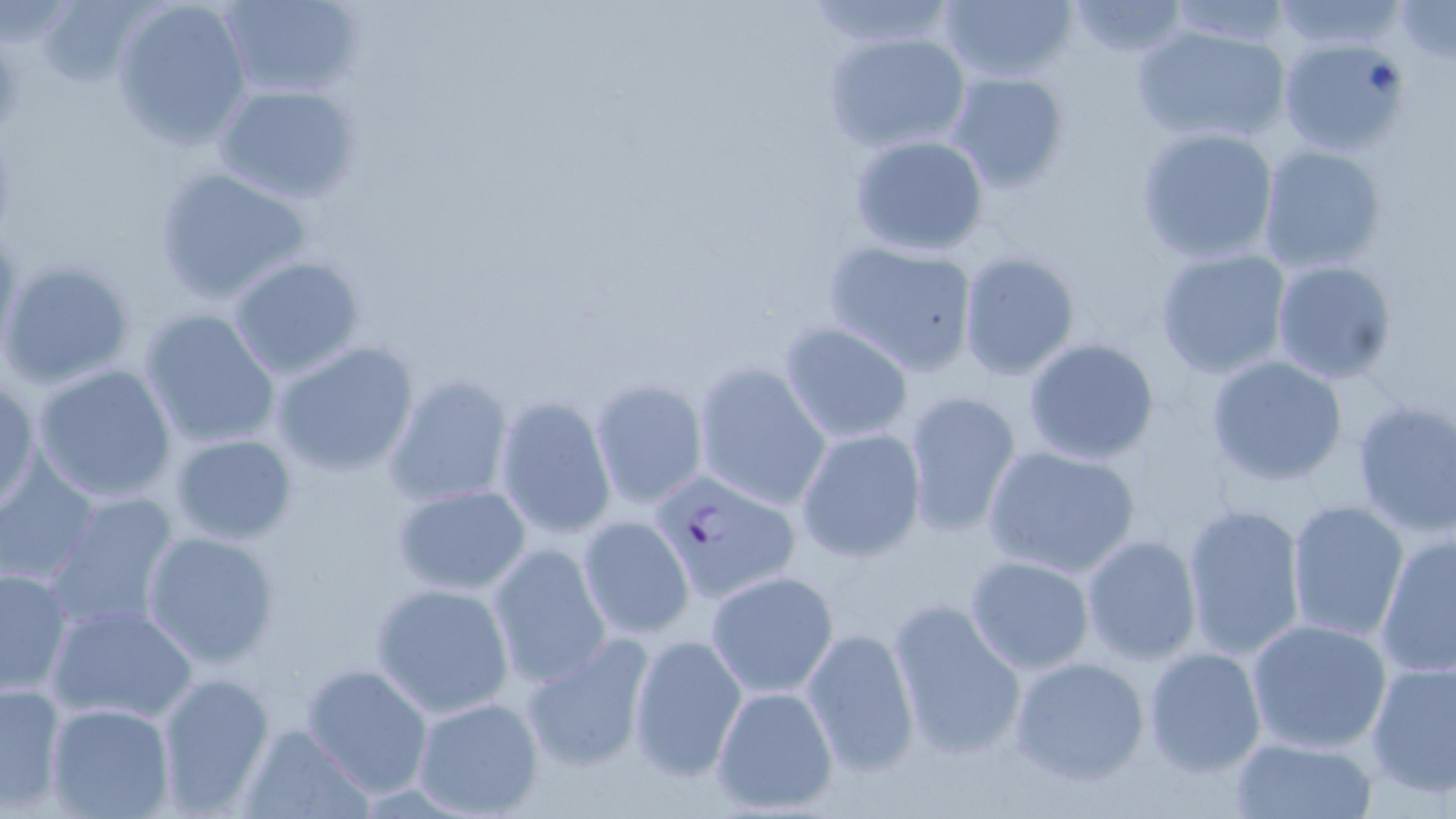

Summary:
  - Coordinate format: approximate bounding boxes as (x1,y1)-(x2,y2) corner pairs in pixels
  - Uninfected red blood cell locations: (110,0)-(254,150), (215,0)-(365,103), (935,0)-(1079,85), (802,1)-(961,51), (1061,1)-(1192,57), (1161,1)-(1297,49), (1267,1)-(1406,51), (1393,2)-(1456,66), (32,3)-(152,91), (1130,23)-(1291,149), (822,30)-(973,155), (1277,38)-(1410,157), (1,43)-(29,134), (945,70)-(1072,195), (212,82)-(361,204), (1134,125)-(1280,266), (847,132)-(991,259), (1256,144)-(1389,274), (153,164)-(317,304), (821,238)-(982,375), (1153,247)-(1294,379), (957,250)-(1082,381), (227,254)-(366,380), (1269,261)-(1398,384), (139,308)-(282,450), (778,321)-(916,445), (1022,337)-(1163,467), (270,340)-(420,479), (1205,354)-(1349,488), (693,364)-(831,509), (32,365)-(178,504), (383,374)-(516,509), (0,378)-(38,512), (590,379)-(707,508), (901,389)-(1023,538), (492,395)-(617,539), (1349,397)-(1456,538), (794,427)-(926,563), (168,432)-(299,543), (981,443)-(1142,577), (0,459)-(101,587), (392,483)-(533,595), (43,490)-(182,637), (1286,499)-(1410,645), (1182,503)-(1307,662), (578,516)-(694,640), (140,529)-(282,669), (1375,532)-(1456,679), (1080,535)-(1202,665), (488,542)-(613,688), (965,554)-(1095,674), (0,566)-(73,699), (705,569)-(839,698), (370,582)-(516,717), (886,597)-(1028,761), (46,602)-(199,726), (1246,619)-(1393,755), (801,626)-(920,776), (519,633)-(657,774), (625,633)-(748,781), (1141,646)-(1268,777), (1008,654)-(1150,788), (1365,659)-(1456,797), (299,662)-(435,799), (152,670)-(276,815), (0,681)-(67,811), (710,686)-(841,814), (411,695)-(545,817), (46,703)-(175,819), (237,724)-(375,819), (1229,735)-(1378,818)
  - Plasmodium falciparum-infected red blood cell locations: (0,259)-(137,390), (650,466)-(803,604)
  - Slide-level diagnosis: Plasmodium falciparum
  - Modality: optical microscopy
  - Field of view: one of a larger specimen
  - Magnification: 1000x
  - Stain: May-Grünwald-Giemsa
  - Preparation: thin blood film
  - Image size: 1456×819 pixels